Assess this cell for malaria.
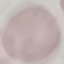

It is uninfected.

Automatically extracted cell patch, resized to 64 × 64 pixels. Photographed with a smartphone camera at the microscope eyepiece. Thin smear of blood. Giemsa stain.